Locate every malaria parasite.
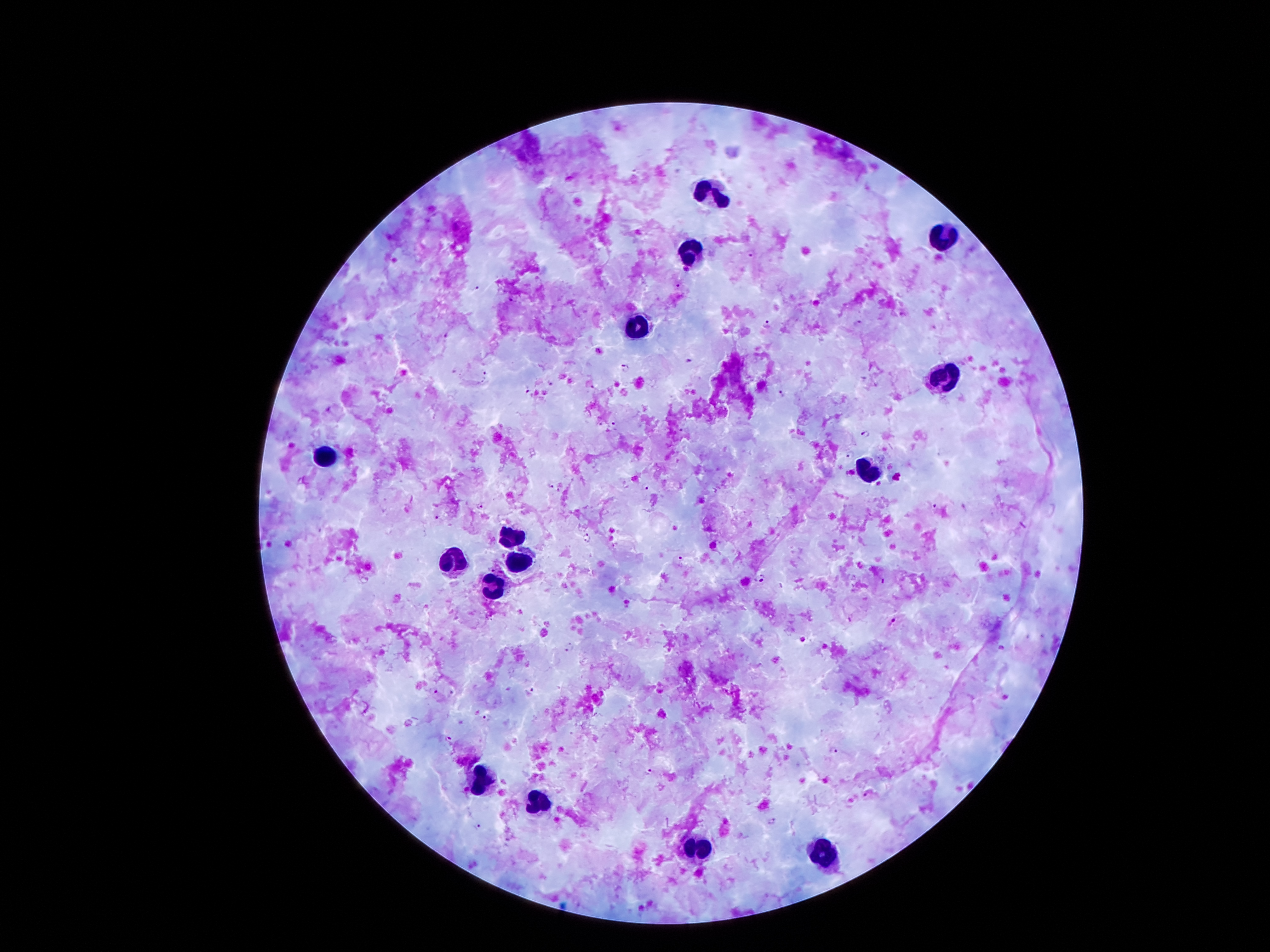

Approximate object centers, in pixels from the top-left corner.
Malaria parasites: (x=751, y=252), (x=476, y=286), (x=678, y=287), (x=858, y=324), (x=768, y=325), (x=444, y=336), (x=688, y=361), (x=625, y=367), (x=484, y=375), (x=550, y=384), (x=593, y=388), (x=527, y=393), (x=782, y=394), (x=614, y=426), (x=866, y=432), (x=849, y=455), (x=646, y=485), (x=549, y=486), (x=559, y=489), (x=481, y=506), (x=936, y=506), (x=437, y=517), (x=589, y=540), (x=680, y=559), (x=759, y=578), (x=895, y=623), (x=569, y=647), (x=533, y=689), (x=453, y=691), (x=436, y=693), (x=486, y=718), (x=447, y=738), (x=833, y=752), (x=649, y=774), (x=867, y=796), (x=772, y=822), (x=478, y=823).

leukocyte locations = (x=712, y=191), (x=945, y=239), (x=689, y=252), (x=638, y=326), (x=944, y=378), (x=329, y=456), (x=867, y=470), (x=510, y=534), (x=455, y=561), (x=521, y=563), (x=493, y=588), (x=481, y=777), (x=539, y=806), (x=699, y=851), (x=821, y=853)
stain = Giemsa
magnification = 100x
field of view = single
capture = smartphone through the microscope eyepiece
preparation = thick blood film
image size = 1270×952 pixels
patient malaria status = infected with Plasmodium falciparum